Mark where platelets are.
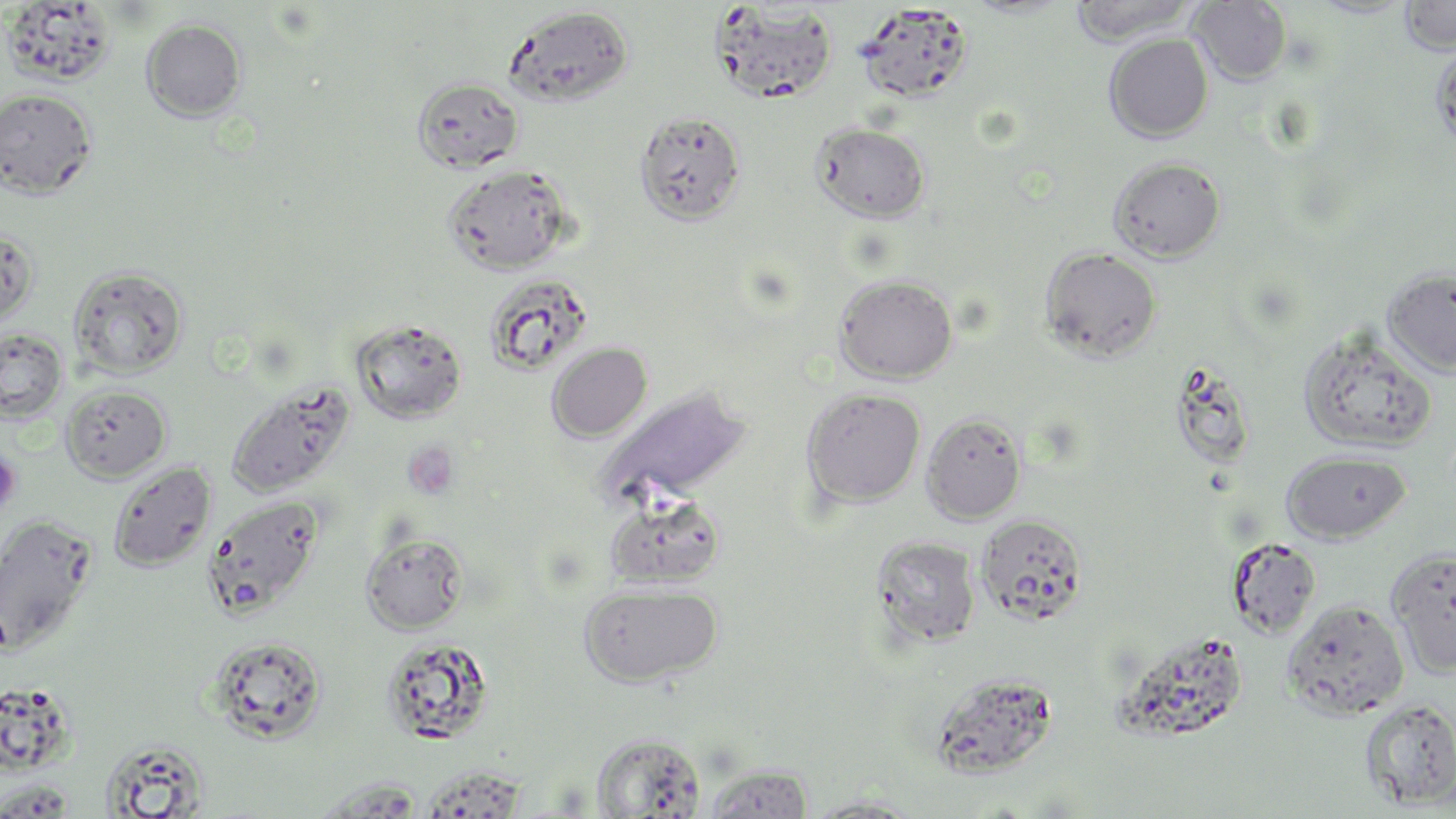
Approximate bounding boxes as named x1/y1/x2/y2 corners in pixels.
Platelets: (x1=403, y1=441, x2=460, y2=501), (x1=0, y1=449, x2=22, y2=514).

Summary:
  - Uninfected red blood cell locations: (x1=1399, y1=0, x2=1456, y2=55), (x1=2, y1=1, x2=119, y2=87), (x1=1069, y1=1, x2=1198, y2=46), (x1=1189, y1=1, x2=1291, y2=85), (x1=855, y1=3, x2=974, y2=103), (x1=707, y1=4, x2=839, y2=104), (x1=503, y1=6, x2=633, y2=108), (x1=141, y1=18, x2=247, y2=122), (x1=1103, y1=33, x2=1214, y2=143), (x1=1431, y1=43, x2=1456, y2=154), (x1=412, y1=76, x2=524, y2=174), (x1=0, y1=89, x2=98, y2=199), (x1=634, y1=109, x2=747, y2=225), (x1=812, y1=123, x2=931, y2=222), (x1=1108, y1=156, x2=1225, y2=262), (x1=442, y1=163, x2=574, y2=275), (x1=0, y1=226, x2=40, y2=328), (x1=1040, y1=246, x2=1162, y2=362), (x1=68, y1=264, x2=189, y2=379), (x1=1382, y1=267, x2=1456, y2=377), (x1=483, y1=274, x2=594, y2=375), (x1=834, y1=274, x2=957, y2=383), (x1=349, y1=318, x2=468, y2=424), (x1=1297, y1=327, x2=1437, y2=456), (x1=0, y1=328, x2=68, y2=423), (x1=546, y1=342, x2=652, y2=442), (x1=1170, y1=360, x2=1258, y2=470), (x1=226, y1=378, x2=356, y2=498), (x1=60, y1=384, x2=171, y2=482), (x1=596, y1=386, x2=753, y2=507), (x1=801, y1=387, x2=926, y2=508), (x1=921, y1=411, x2=1027, y2=524), (x1=1281, y1=450, x2=1411, y2=543), (x1=107, y1=461, x2=217, y2=572), (x1=605, y1=493, x2=727, y2=588), (x1=202, y1=494, x2=325, y2=618), (x1=0, y1=514, x2=99, y2=655), (x1=976, y1=514, x2=1088, y2=625), (x1=360, y1=530, x2=469, y2=634), (x1=871, y1=535, x2=982, y2=648), (x1=1226, y1=536, x2=1322, y2=638), (x1=1386, y1=547, x2=1456, y2=677), (x1=578, y1=582, x2=723, y2=687), (x1=1282, y1=599, x2=1409, y2=720), (x1=205, y1=635, x2=328, y2=744), (x1=379, y1=636, x2=494, y2=745), (x1=928, y1=671, x2=1061, y2=778), (x1=1358, y1=698, x2=1456, y2=810), (x1=591, y1=732, x2=705, y2=817), (x1=99, y1=737, x2=211, y2=816), (x1=702, y1=764, x2=814, y2=818), (x1=309, y1=777, x2=426, y2=817), (x1=0, y1=780, x2=77, y2=817), (x1=804, y1=796, x2=924, y2=818)
  - Slide-level diagnosis: negative for blood parasites
  - Preparation: thin blood film
  - Field of view: one of a larger specimen
  - Magnification: 1000x
  - Image size: 1456×819 pixels
  - Stain: May-Grünwald-Giemsa
  - Modality: optical microscopy